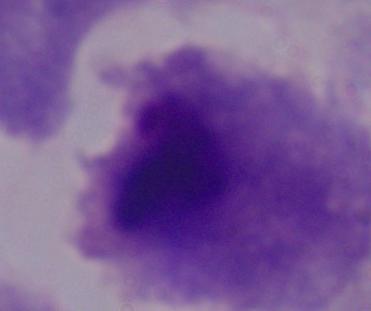
A trichomonad is shown. Captured at 1000x magnification. Photomicrograph.